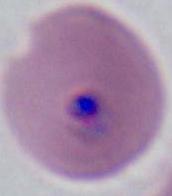
Summary:
  - Identification: Plasmodium
  - Magnification: 400x or 1000x
  - Modality: photomicrograph